Name the parasite shown.
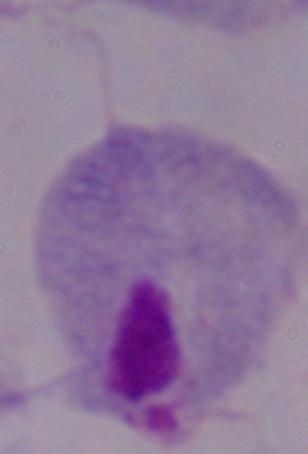

This is a trichomonad.

Summary:
  - Magnification: 1000x
  - Modality: photomicrograph